Assess this cell for malaria.
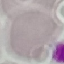
It is uninfected.

Summary:
  - Image type: automatically extracted cell patch, resized to 64 × 64 pixels
  - Preparation: thin blood smear
  - Stain: Giemsa
  - Capture: smartphone through the microscope eyepiece